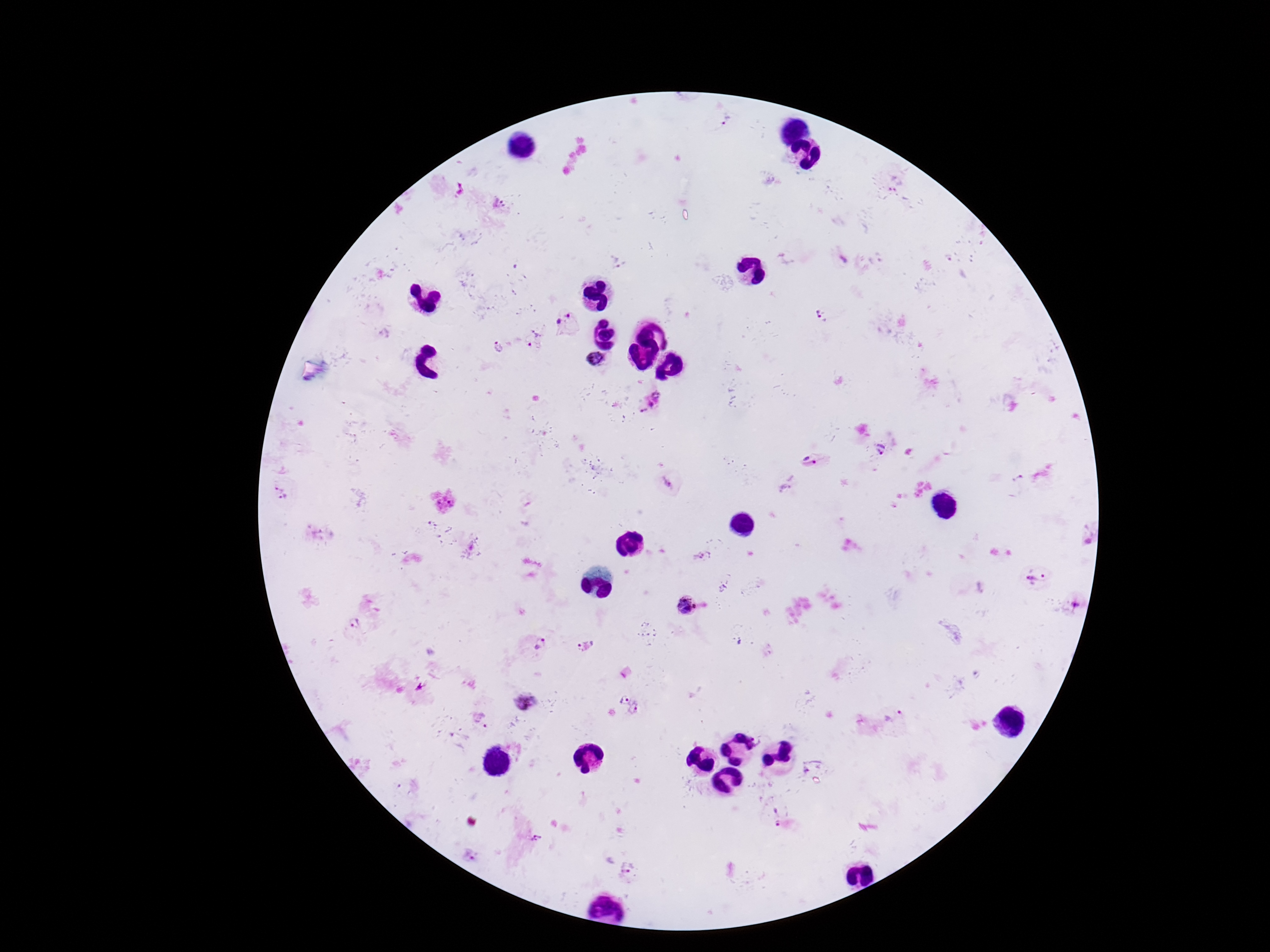

Approximate centers as {x, y} in pixels. Plasmodium parasite locations: {727, 122}, {895, 184}, {499, 203}, {568, 314}, {823, 316}, {559, 322}, {538, 332}, {530, 345}, {498, 348}, {595, 359}, {657, 394}, {651, 405}, {643, 411}, {880, 449}, {809, 461}, {1020, 478}, {667, 482}, {276, 488}, {284, 499}, {699, 556}, {1037, 579}, {686, 606}, {355, 622}, {537, 643}, {585, 644}, {624, 697}, {523, 702}, {636, 709}, {894, 716}, {482, 719}, {809, 762}, {776, 815}, {536, 838}, {627, 868}. Patient malaria status: infected. Thick blood smear. Photographed through the microscope eyepiece with a smartphone camera. Image is 1270×952 pixels. Giemsa-stained preparation. 100x magnification. Single field of view.